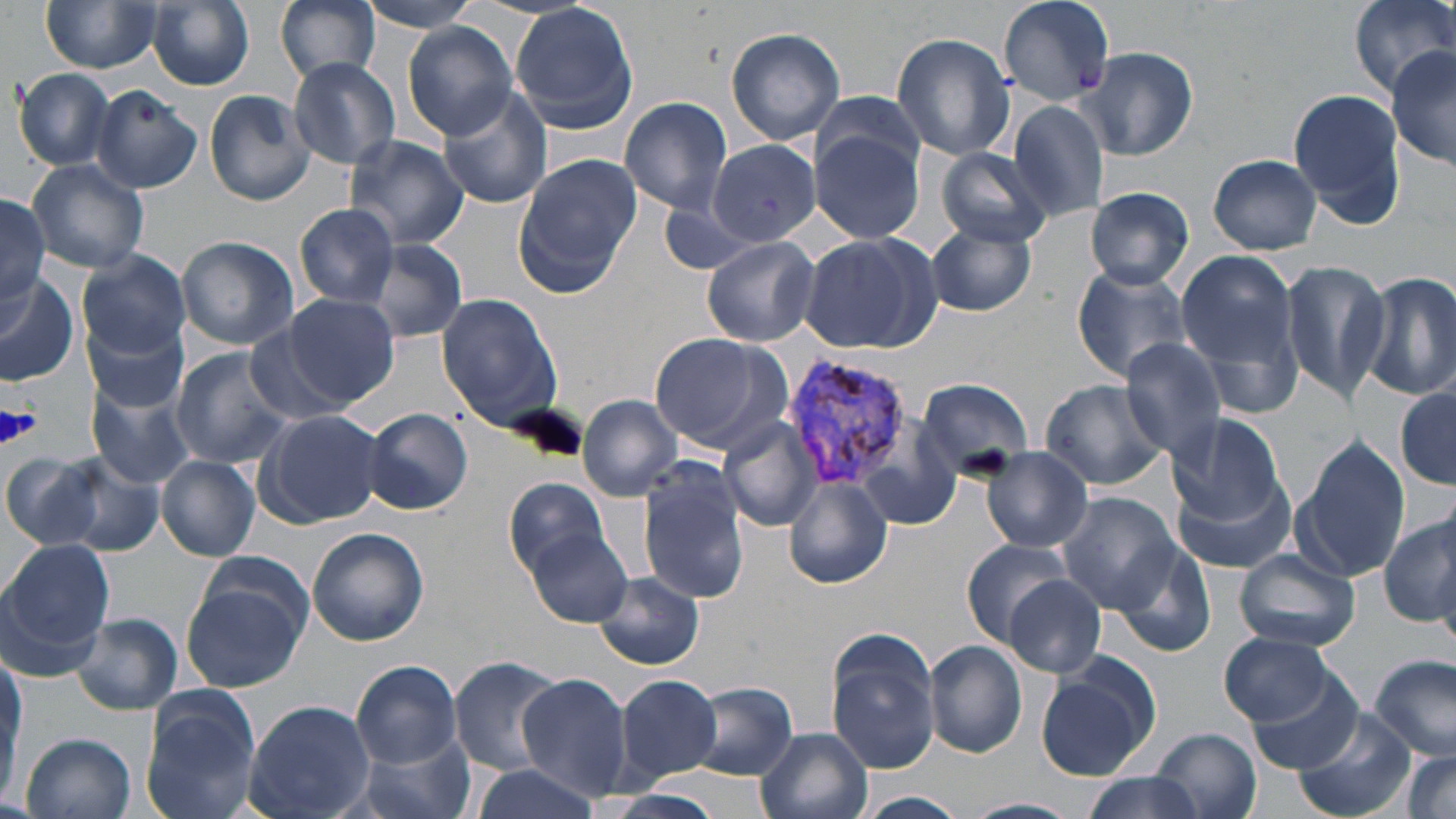

slide-level diagnosis = Plasmodium vivax
magnification = 1000x
image size = 1456×819 pixels
Plasmodium vivax-infected red blood cell locations = approximate bounding boxes as [x1, y1, x2, y2] in pixels: [783, 356, 914, 492]
stain = May-Grünwald-Giemsa
preparation = thin blood smear
platelet locations = approximate bounding boxes as [x1, y1, x2, y2] in pixels: [1, 404, 41, 448]
field of view = one of a larger specimen
uninfected red blood cell locations = approximate bounding boxes as [x1, y1, x2, y2] in pixels: [273, 0, 384, 88], [996, 0, 1116, 109], [1351, 0, 1456, 95], [40, 1, 164, 74], [355, 1, 488, 33], [149, 2, 254, 90], [509, 5, 641, 134], [403, 25, 519, 138], [726, 27, 847, 144], [891, 32, 1017, 162], [1087, 46, 1199, 162], [1387, 46, 1455, 169], [288, 58, 401, 169], [12, 68, 115, 170], [92, 86, 202, 193], [1286, 88, 1406, 228], [203, 89, 316, 206], [438, 89, 553, 208], [811, 91, 927, 180], [621, 97, 732, 213], [1005, 98, 1110, 224], [811, 128, 926, 246], [343, 133, 469, 250], [708, 141, 821, 249], [932, 147, 1052, 249], [513, 153, 641, 290], [1208, 154, 1323, 253], [27, 160, 150, 275], [1081, 187, 1194, 288], [0, 196, 51, 305], [656, 198, 763, 276], [295, 204, 399, 306], [926, 223, 1039, 317], [175, 235, 298, 349], [700, 235, 819, 347], [800, 236, 930, 353], [359, 238, 469, 344], [1175, 248, 1308, 405], [79, 253, 191, 356], [1279, 260, 1392, 404], [1071, 264, 1197, 384], [1358, 272, 1456, 402], [0, 274, 80, 385], [279, 292, 400, 409], [436, 294, 563, 429], [83, 316, 187, 411], [245, 326, 352, 428], [647, 332, 791, 455], [1120, 338, 1231, 462], [169, 348, 295, 467], [914, 377, 1034, 477], [1038, 379, 1171, 491], [87, 381, 193, 488], [1395, 385, 1455, 489], [577, 393, 682, 500], [365, 407, 473, 515], [256, 408, 387, 528], [1167, 410, 1288, 520], [719, 417, 825, 531], [1294, 435, 1412, 582], [981, 448, 1094, 552], [0, 450, 109, 552], [36, 454, 164, 557], [155, 456, 261, 561], [637, 465, 751, 605], [1173, 472, 1298, 574], [504, 476, 612, 579], [784, 476, 893, 589], [1055, 492, 1180, 612], [1379, 511, 1454, 626], [306, 528, 428, 647], [527, 529, 632, 627], [1109, 536, 1217, 660], [960, 538, 1077, 646], [0, 540, 114, 672], [1236, 547, 1359, 653], [180, 566, 310, 695], [996, 569, 1105, 675], [592, 572, 703, 670], [73, 615, 182, 715], [1220, 632, 1339, 727], [824, 635, 940, 774], [924, 640, 1027, 758], [1368, 655, 1455, 762], [450, 657, 563, 777], [352, 660, 464, 767], [1036, 661, 1156, 780], [1246, 667, 1362, 775], [0, 668, 25, 798], [516, 672, 633, 800], [616, 674, 724, 781], [690, 683, 798, 781], [140, 688, 262, 819], [242, 699, 375, 819], [1297, 704, 1417, 819], [755, 727, 873, 819], [1151, 727, 1262, 819], [20, 732, 136, 819], [354, 736, 473, 819], [1401, 752, 1454, 818], [469, 764, 606, 819], [1078, 770, 1207, 819], [855, 792, 969, 818], [963, 797, 1079, 819]
modality = optical microscopy